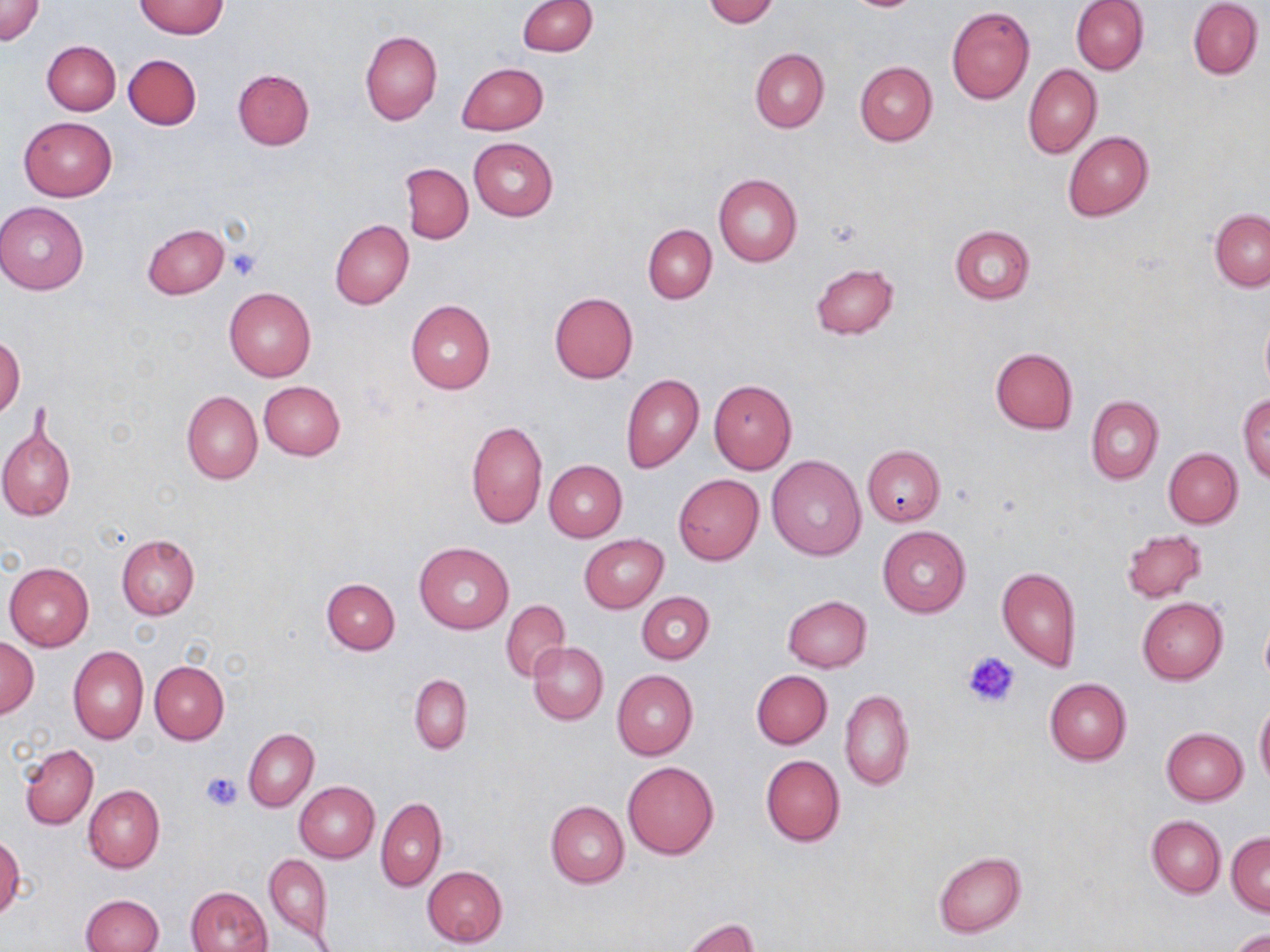

Approximate bounding boxes as (x1,y1)-(x2,y2) corner pairs in pixels. Uninfected red blood cell locations: (519,0)-(597,56), (705,0)-(778,26), (1072,0)-(1149,75), (1188,0)-(1262,79), (1,1)-(44,46), (136,1)-(227,39), (849,1)-(920,11), (946,6)-(1035,104), (360,29)-(442,125), (43,40)-(121,115), (750,49)-(828,132), (123,54)-(201,130), (854,60)-(937,145), (457,63)-(549,134), (1023,65)-(1102,158), (233,68)-(315,150), (19,116)-(116,200), (1063,131)-(1153,221), (469,137)-(558,221), (401,163)-(474,243), (713,173)-(802,265), (1,202)-(89,294), (1210,209)-(1270,290), (329,219)-(414,310), (143,223)-(230,299), (949,224)-(1035,305), (643,225)-(716,302), (810,262)-(898,340), (224,287)-(316,381), (548,291)-(638,384), (406,300)-(495,394), (1260,315)-(1270,394), (0,335)-(25,419), (989,348)-(1079,434), (620,373)-(704,473), (708,379)-(796,476), (259,381)-(346,461), (181,391)-(262,484), (1238,393)-(1270,483), (1085,396)-(1163,484), (0,418)-(76,522), (465,420)-(548,529), (862,446)-(945,527), (1164,448)-(1242,528), (767,455)-(867,562), (544,460)-(626,541), (674,474)-(764,565), (877,526)-(970,618), (1120,529)-(1207,602), (116,534)-(199,620), (579,534)-(668,612), (413,543)-(514,635), (4,562)-(94,651), (996,565)-(1082,673), (322,577)-(400,654), (637,591)-(714,663), (783,595)-(871,671), (1138,596)-(1227,684), (501,598)-(571,682), (1259,611)-(1270,688), (1,638)-(39,717), (528,642)-(608,725), (67,645)-(147,744), (150,661)-(228,744), (612,669)-(697,761), (751,670)-(832,749), (409,673)-(471,755), (1044,677)-(1132,766), (839,689)-(915,790), (1255,703)-(1270,788), (243,728)-(318,811), (1162,728)-(1247,805), (19,744)-(98,830), (760,754)-(846,846), (622,761)-(718,860), (296,782)-(380,862), (83,784)-(164,873), (376,796)-(447,891), (545,801)-(629,888), (1147,816)-(1225,897), (1227,833)-(1270,915), (1,834)-(24,922), (933,850)-(1026,938), (263,852)-(333,945), (422,865)-(507,947), (186,886)-(272,952), (80,894)-(163,952), (683,916)-(759,952), (1226,928)-(1270,952). Platelet locations: (226,248)-(260,280), (963,650)-(1021,707), (201,770)-(242,811). Slide-level diagnosis: no evidence of blood parasites. Captured at 1000x magnification. May-Grünwald-Giemsa stain. Optical microscopy. Thin blood film. One field of a larger specimen. Image is 1270×952 pixels.